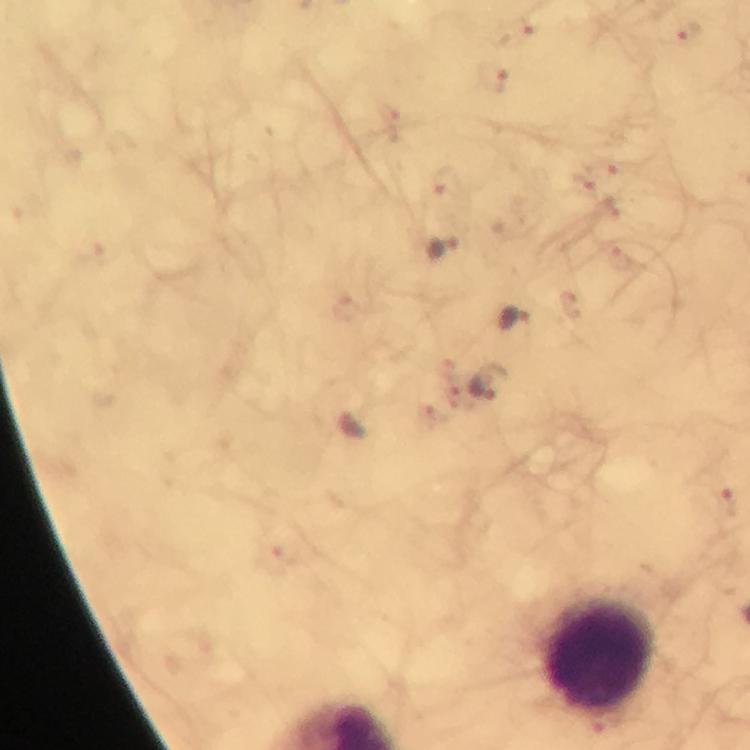
Approximate object centers, in pixels from the top-left corner.
Summary:
  - Malaria parasite locations: (x=688, y=33), (x=495, y=79), (x=447, y=186), (x=447, y=249), (x=515, y=319), (x=489, y=383), (x=728, y=501)
  - Leukocyte locations: (x=596, y=655)
  - Image size: 750×750 pixels
  - Preparation: thick blood smear
  - Context: from a diagnostic examination for malaria
  - Immersion oil: applied
  - Cropped from: one field of view
  - Capture: smartphone mounted on the microscope
  - Stain: Giemsa
  - Magnification: 100x